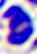

Micrograph. 400x magnification. A white blood cell is seen.